Assess this cell for malaria.
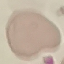

Uninfected.

Summary:
  - Image type: cell patch, automatically extracted from a larger field of view and resized to 64 × 64 pixels
  - Stain: Giemsa
  - Capture: smartphone camera at the microscope eyepiece
  - Preparation: thin smear